Locate every Plasmodium parasite.
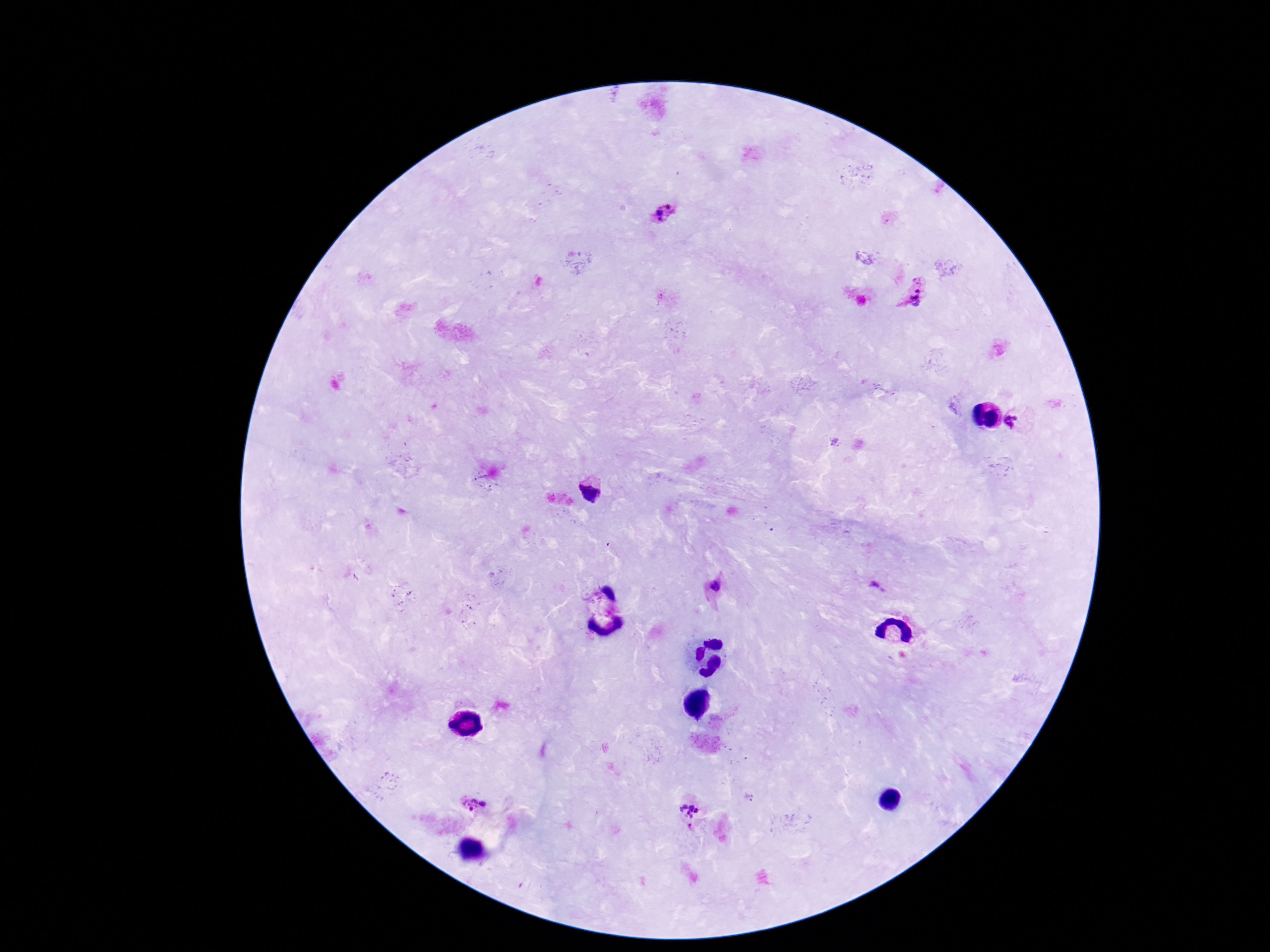
Approximate centers as {x, y} in pixels.
Plasmodium parasites: {664, 214}, {917, 290}, {1022, 422}, {594, 489}, {715, 585}, {876, 587}, {468, 804}, {487, 806}, {689, 811}.

Photographed through the microscope eyepiece with a smartphone camera. 100x magnification. Thick blood film. Patient malaria status: positive. Single field of view. Image is 1270×952 pixels. Giemsa-stained preparation.